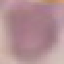
result = negative for malaria parasites
stain = Giemsa
image type = automatically extracted cell patch, resized to 64 × 64 pixels
capture = smartphone camera at the microscope eyepiece
preparation = thin smear